Report the malaria status.
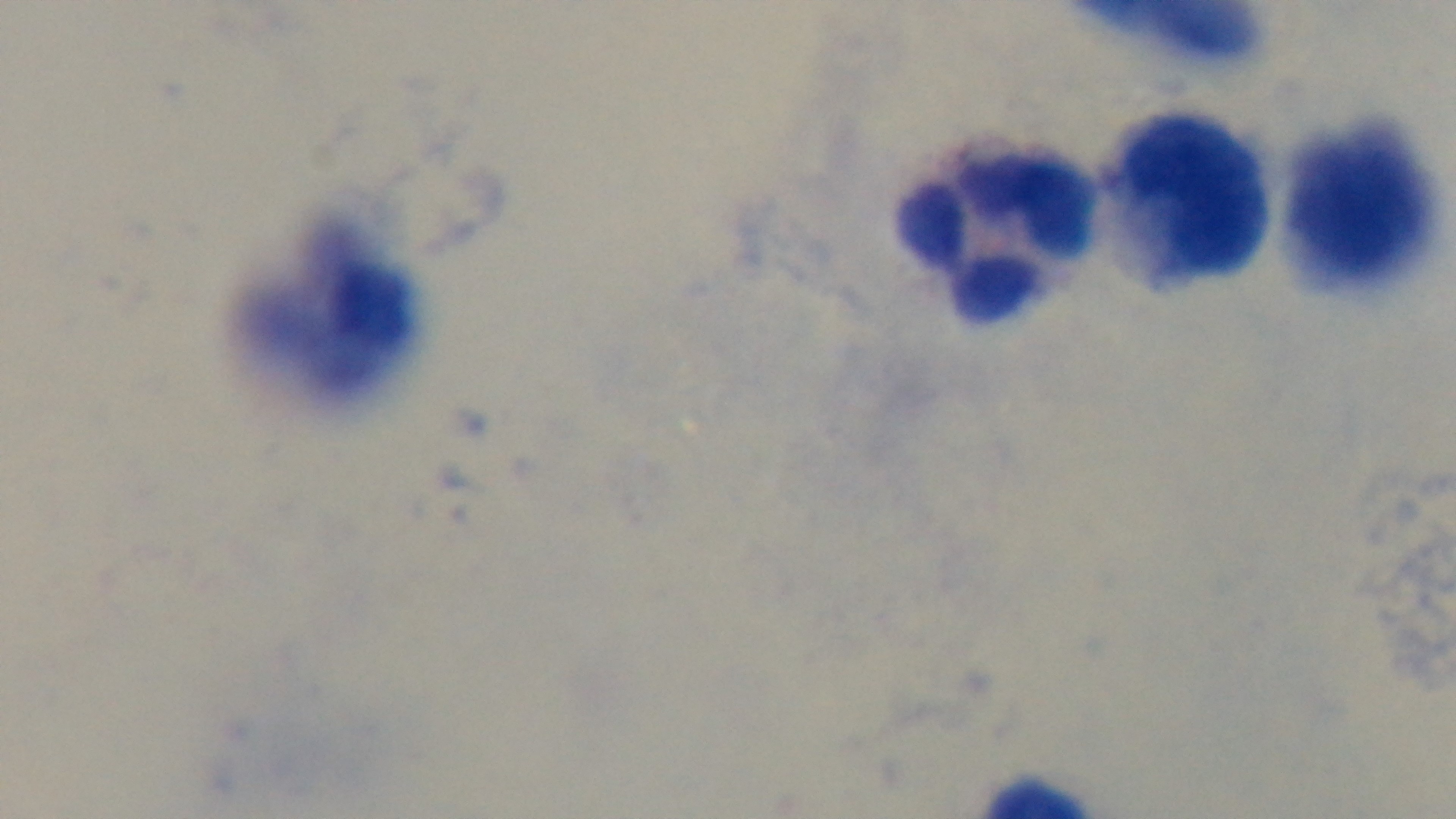
Uninfected.

Giemsa-stained. Captured with a mounted 4K digital camera. Photomicrograph. One field from the slide. Preparation: thick smear. 100x oil-immersion objective.